Classify this cell by malaria status.
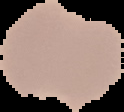
Parasitized.

From a thin blood smear. The area outside the segmented cell region is set to black. Image is 124×112 pixels.